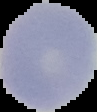

Summary:
  - Image type: segmented cell region on a black background
  - Result: no malaria parasites detected
  - Preparation: thin blood film
  - Image size: 97×112 pixels